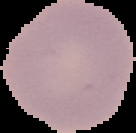
{
  "image_size": "136×133 pixels",
  "result": "no malaria parasites seen",
  "preparation": "thin blood smear",
  "image_type": "segmented cell region with the area outside set to black"
}